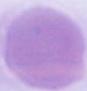 An erythrocyte is seen. Micrograph. Captured at 1000x magnification.